Give the extent of all Trypanosoma brucei.
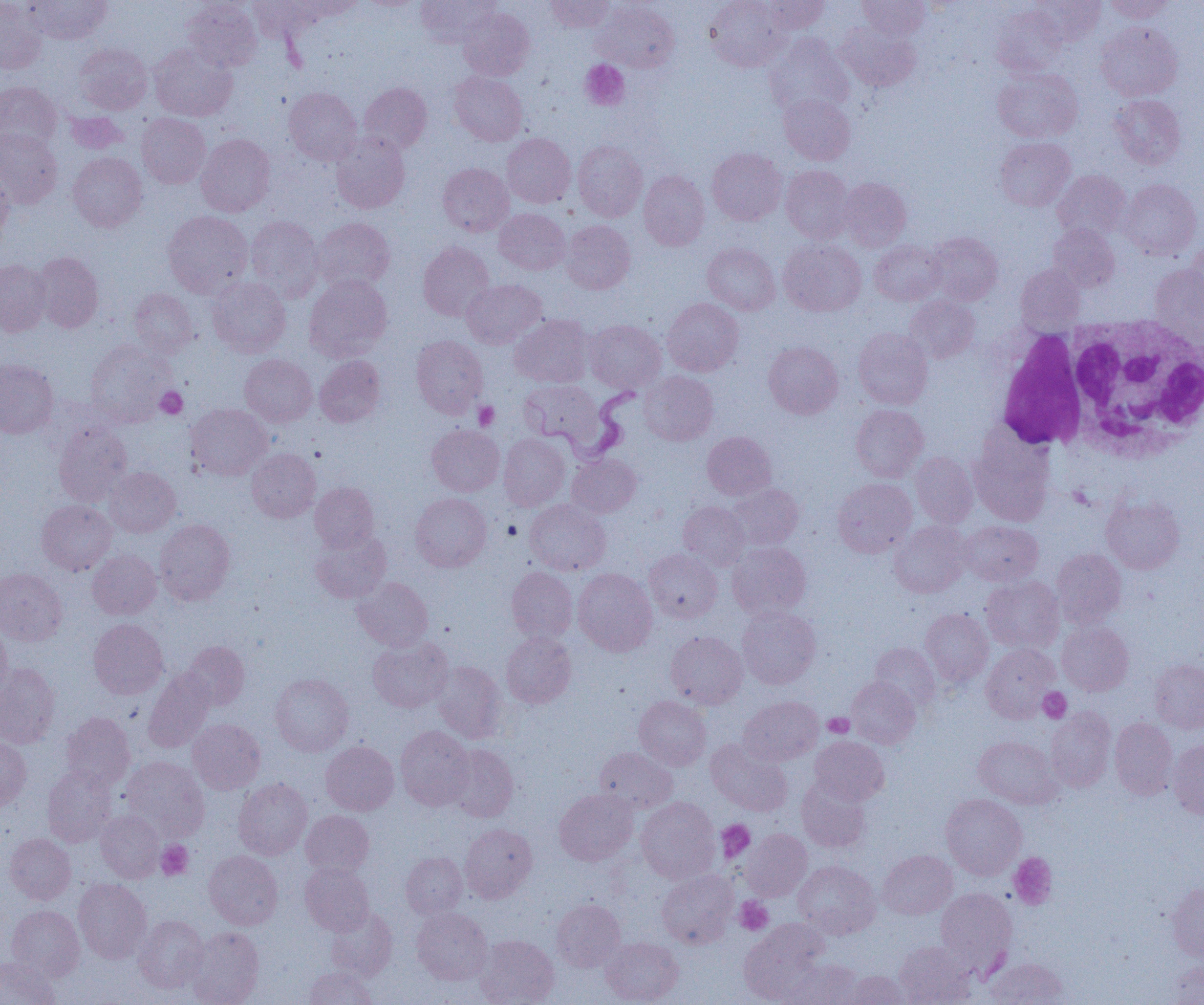
Approximate bounding boxes as (x1, y1, x2, y2) in pixels.
Trypanosoma brucei: (538, 383, 639, 464).

{
  "slide_level_diagnosis": "Trypanosoma brucei",
  "modality": "light microscopy",
  "white_blood_cell_locations": "approximate bounding boxes as (x1, y1, x2, y2) in pixels: (1066, 316, 1204, 460), (995, 328, 1089, 451)",
  "preparation": "thin blood film",
  "image_size": "1204×1005 pixels",
  "uninfected_red_blood_cell_locations": "approximate bounding boxes as (x1, y1, x2, y2) in pixels: (24, 0, 111, 44), (248, 0, 325, 42), (293, 0, 366, 21), (416, 0, 499, 47), (546, 0, 614, 32), (705, 0, 790, 71), (761, 0, 830, 33), (858, 0, 930, 40), (1029, 0, 1105, 46), (1105, 0, 1175, 23), (0, 1, 47, 74), (182, 1, 262, 71), (592, 1, 680, 72), (992, 4, 1066, 77), (458, 7, 535, 80), (834, 21, 920, 91), (1096, 21, 1182, 100), (764, 33, 854, 117), (74, 43, 152, 114), (149, 43, 237, 121), (993, 67, 1083, 142), (449, 71, 527, 146), (0, 81, 61, 150), (359, 82, 432, 154), (284, 87, 362, 165), (779, 93, 855, 164), (1109, 94, 1186, 169), (64, 111, 130, 154), (137, 113, 211, 188), (0, 128, 62, 208), (331, 131, 410, 213), (196, 133, 275, 216), (502, 133, 575, 207), (995, 137, 1076, 211), (573, 140, 647, 221), (707, 148, 786, 225), (68, 152, 147, 232), (437, 163, 513, 236), (781, 165, 854, 243), (1053, 169, 1130, 241), (639, 170, 709, 250), (0, 171, 14, 245), (838, 178, 911, 250), (1118, 179, 1202, 261), (494, 208, 570, 274), (162, 210, 252, 298), (246, 216, 324, 301), (313, 218, 395, 292), (561, 220, 635, 294), (1048, 223, 1120, 292), (926, 231, 1003, 305), (778, 238, 866, 316), (870, 240, 945, 305), (418, 242, 494, 320), (1184, 242, 1204, 313), (702, 243, 780, 315), (31, 251, 104, 333), (0, 259, 51, 336), (1016, 264, 1085, 330), (1149, 265, 1203, 342), (304, 275, 392, 361), (208, 277, 290, 357), (462, 279, 546, 348), (128, 288, 199, 357), (905, 295, 979, 363), (662, 298, 743, 376), (511, 314, 593, 388), (585, 319, 666, 392), (853, 328, 933, 409), (411, 335, 488, 418), (85, 339, 172, 427), (764, 341, 843, 419), (240, 354, 317, 426), (315, 355, 386, 427), (0, 358, 58, 438), (640, 371, 718, 445), (519, 380, 602, 445), (185, 404, 272, 480), (851, 404, 928, 481), (53, 421, 132, 506), (427, 425, 504, 496), (702, 431, 776, 499), (499, 433, 570, 511), (969, 434, 1055, 525), (247, 449, 320, 522), (911, 452, 978, 527), (567, 454, 641, 517), (104, 467, 180, 537), (833, 478, 917, 557), (310, 482, 379, 551), (727, 483, 804, 550), (410, 493, 491, 572), (1101, 496, 1184, 574), (525, 499, 610, 575), (37, 500, 115, 575), (679, 502, 749, 570), (155, 519, 235, 605), (960, 520, 1042, 586), (890, 521, 971, 597), (311, 530, 391, 603), (728, 541, 811, 618), (1051, 548, 1126, 629), (645, 549, 722, 622), (87, 550, 161, 619), (506, 567, 577, 643), (0, 568, 67, 645), (573, 568, 657, 655), (981, 576, 1064, 653), (353, 577, 433, 651), (737, 606, 821, 688), (920, 608, 993, 686), (89, 618, 168, 699), (1057, 620, 1133, 695), (0, 623, 12, 698), (666, 631, 747, 708), (501, 632, 576, 707), (367, 637, 453, 712), (181, 641, 250, 710), (869, 643, 940, 710), (981, 643, 1060, 722), (1150, 659, 1204, 733), (431, 661, 507, 743), (0, 663, 60, 748), (144, 667, 214, 752), (270, 673, 354, 756), (847, 676, 921, 748), (634, 695, 711, 770), (739, 696, 823, 765), (1046, 708, 1116, 792), (61, 712, 135, 790), (1110, 718, 1178, 799), (188, 719, 265, 794), (396, 725, 474, 810), (810, 736, 889, 805), (974, 736, 1061, 808), (0, 738, 31, 810), (707, 739, 792, 816), (1168, 739, 1204, 819), (321, 741, 399, 815), (445, 743, 519, 821), (594, 747, 677, 813), (121, 756, 209, 840), (42, 766, 117, 846), (797, 777, 871, 852), (234, 778, 312, 859), (554, 789, 637, 866), (941, 793, 1026, 879), (636, 797, 720, 883), (96, 810, 165, 882), (301, 810, 374, 877), (460, 823, 537, 903), (742, 829, 812, 900), (4, 834, 76, 904), (204, 850, 283, 929), (878, 850, 957, 919), (401, 852, 467, 918), (794, 860, 880, 938), (300, 863, 374, 935), (657, 870, 737, 947), (73, 878, 151, 963), (1167, 883, 1204, 961), (935, 888, 1017, 974), (552, 899, 624, 971), (7, 905, 84, 980), (326, 907, 398, 981), (412, 907, 492, 985), (134, 915, 209, 993), (739, 920, 829, 1003), (187, 926, 264, 1005), (475, 934, 559, 1005), (601, 937, 683, 1004), (893, 941, 976, 1005), (0, 956, 59, 1005), (985, 957, 1068, 1004), (782, 958, 862, 1005), (1166, 960, 1204, 1005), (304, 967, 378, 1005), (841, 970, 912, 1004)",
  "platelet_locations": "approximate bounding boxes as (x1, y1, x2, y2) in pixels: (580, 60, 629, 110), (155, 386, 187, 419), (474, 401, 499, 430), (1038, 688, 1071, 723), (823, 712, 854, 737), (716, 820, 755, 862), (157, 841, 193, 880), (1009, 852, 1057, 909), (735, 897, 773, 935)",
  "magnification": "1000x",
  "field_of_view": "one of a larger specimen"
}